Locate every leukocyte (white blood cell).
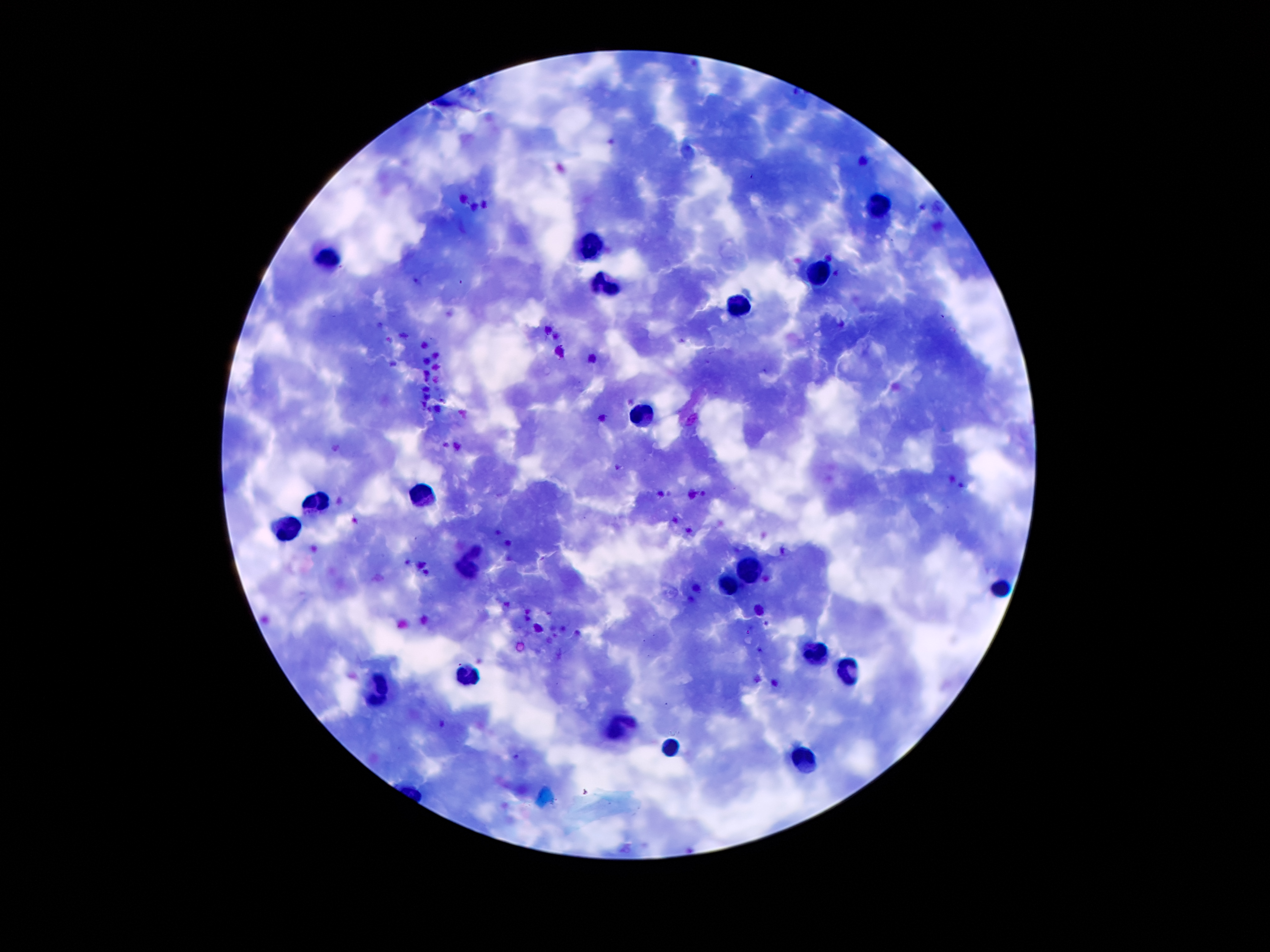

Approximate centers as [x, y] in pixels.
Leukocytes: [878, 206], [590, 245], [324, 257], [811, 276], [604, 282], [738, 309], [638, 415], [419, 499], [316, 505], [288, 525], [470, 566], [747, 567], [724, 584], [999, 586], [817, 656], [467, 674], [850, 674], [374, 693], [621, 727], [668, 746], [800, 752].

Plasmodium parasite locations = [617, 467], [355, 521]
preparation = thick blood smear
magnification = 100x
stain = Giemsa
patient malaria status = infected with Plasmodium falciparum
field of view = single
image size = 1270×952 pixels
capture = smartphone through the microscope eyepiece